Give the location of every parasitized red blood cell.
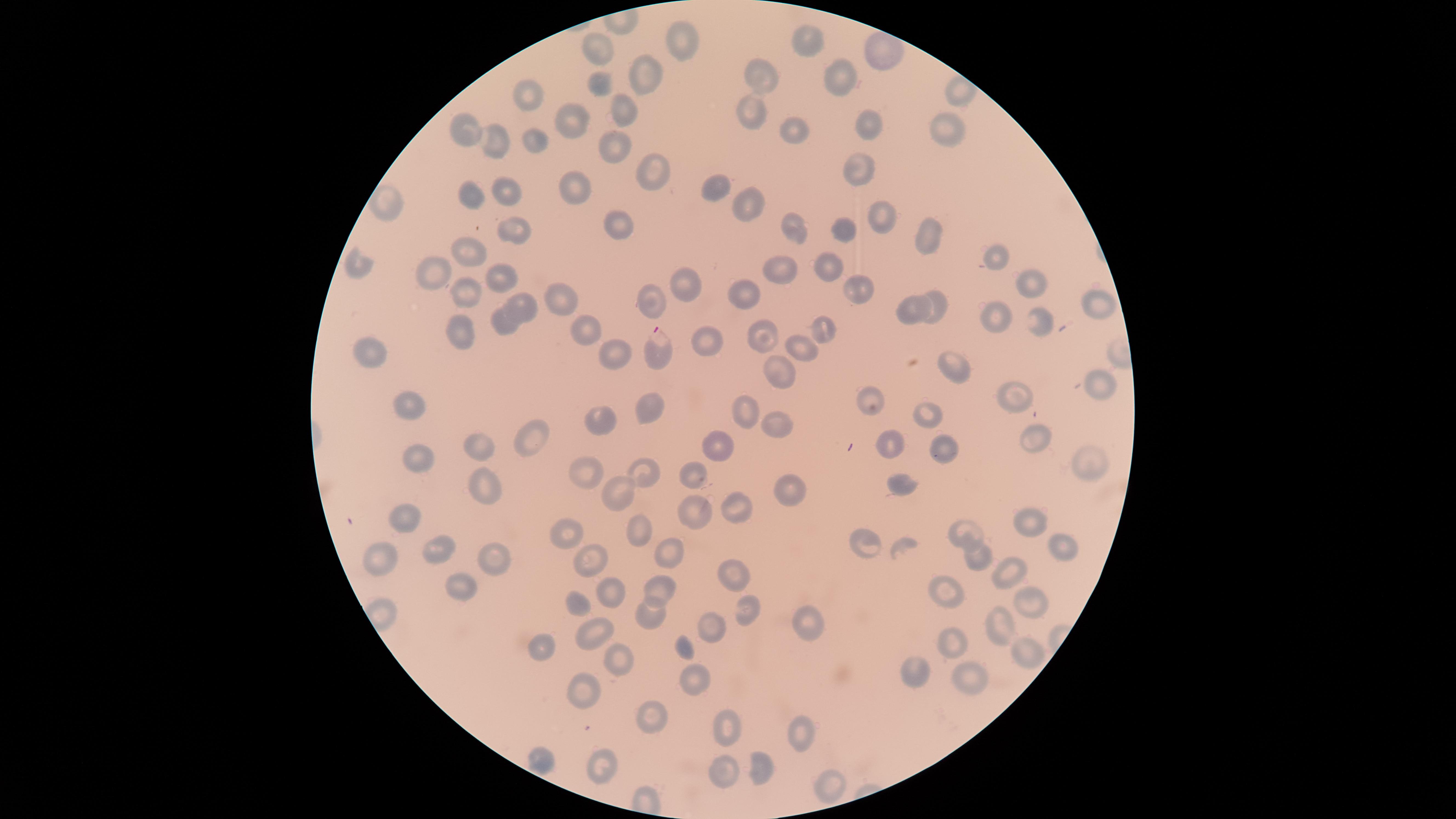

Approximate marker points as {x, y} in pixels.
Parasitized red blood cells: {654, 344}.

Approximate marker points as {x, y} in pixels. Uninfected red blood cells: {799, 37}, {680, 42}, {599, 49}, {647, 75}, {760, 79}, {594, 80}, {843, 80}, {528, 100}, {618, 107}, {752, 109}, {865, 119}, {567, 124}, {467, 125}, {947, 131}, {797, 134}, {537, 142}, {501, 143}, {608, 146}, {650, 168}, {866, 173}, {716, 186}, {471, 191}, {497, 191}, {578, 192}, {745, 198}, {393, 204}, {877, 217}, {619, 218}, {506, 225}, {796, 227}, {845, 230}, {927, 233}, {466, 247}, {997, 252}, {784, 265}, {831, 266}, {431, 269}, {351, 270}, {496, 275}, {1026, 277}, {680, 281}, {855, 289}, {746, 290}, {468, 294}, {556, 298}, {651, 301}, {519, 303}, {936, 306}, {1098, 306}, {908, 307}, {995, 314}, {821, 318}, {506, 320}, {1035, 324}, {590, 333}, {465, 334}, {761, 334}, {711, 338}, {804, 351}, {369, 355}, {614, 356}, {952, 366}, {785, 372}, {1103, 387}, {1011, 395}, {869, 396}, {405, 401}, {657, 410}, {743, 411}, {931, 413}, {608, 421}, {777, 429}, {533, 431}, {1037, 436}, {894, 443}, {488, 445}, {940, 446}, {718, 450}, {1089, 457}, {418, 460}, {642, 473}, {691, 473}, {593, 476}, {487, 485}, {898, 485}, {789, 489}, {614, 494}, {695, 509}, {736, 509}, {409, 523}, {1031, 524}, {964, 526}, {640, 530}, {574, 535}, {863, 544}, {1061, 545}, {440, 550}, {672, 552}, {979, 557}, {386, 559}, {586, 559}, {495, 565}, {1000, 567}, {734, 576}, {460, 582}, {658, 585}, {611, 591}, {951, 594}, {1027, 600}, {750, 607}, {652, 609}, {578, 610}, {808, 619}, {711, 623}, {996, 626}, {594, 633}, {959, 645}, {546, 650}, {1023, 651}, {615, 661}, {970, 672}, {921, 673}, {698, 682}, {585, 690}, {653, 715}, {724, 726}, {803, 735}, {538, 753}, {607, 759}, {759, 770}, {723, 773}, {830, 788}. One field of view of the specimen. Image is 1456×819 pixels. Thin smear of blood. Giemsa stain. Species: Plasmodium falciparum. The visible region is circular. Photographed with a smartphone camera through the microscope eyepiece.